Give the position of every Plasmodium parasite visible.
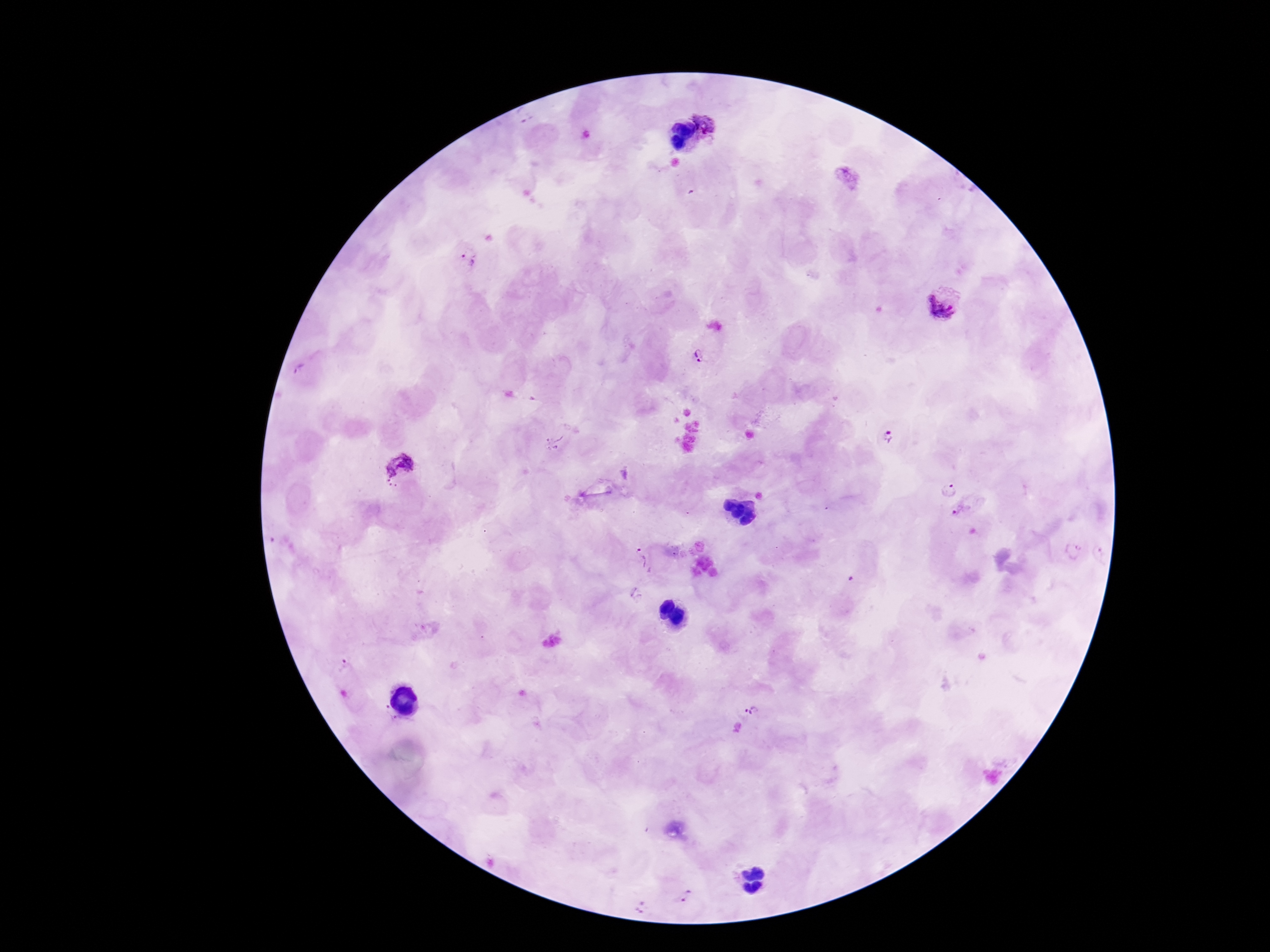
Approximate object centers, in pixels from the top-left corner.
Plasmodium parasites: (x=705, y=121), (x=847, y=178), (x=467, y=258), (x=945, y=304), (x=699, y=354), (x=299, y=372), (x=890, y=437), (x=553, y=442), (x=400, y=470), (x=951, y=490), (x=962, y=511), (x=1074, y=552), (x=644, y=561), (x=344, y=668), (x=386, y=710), (x=752, y=710), (x=400, y=722), (x=683, y=895), (x=644, y=909).

{
  "preparation": "thick blood smear",
  "field_of_view": "one from this slide",
  "capture": "smartphone camera through the microscope eyepiece",
  "magnification": "100x",
  "stain": "Giemsa",
  "image_size": "1270×952 pixels",
  "patient_malaria_status": "infected"
}